Assess this cell for malaria.
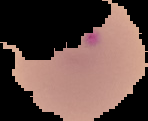
Parasitized.

Cell region segmented out of the field of view; the surrounding area is masked to black. Image is 148×121 pixels. From a thin blood film.